Give the extent of all uninfected red blood cells.
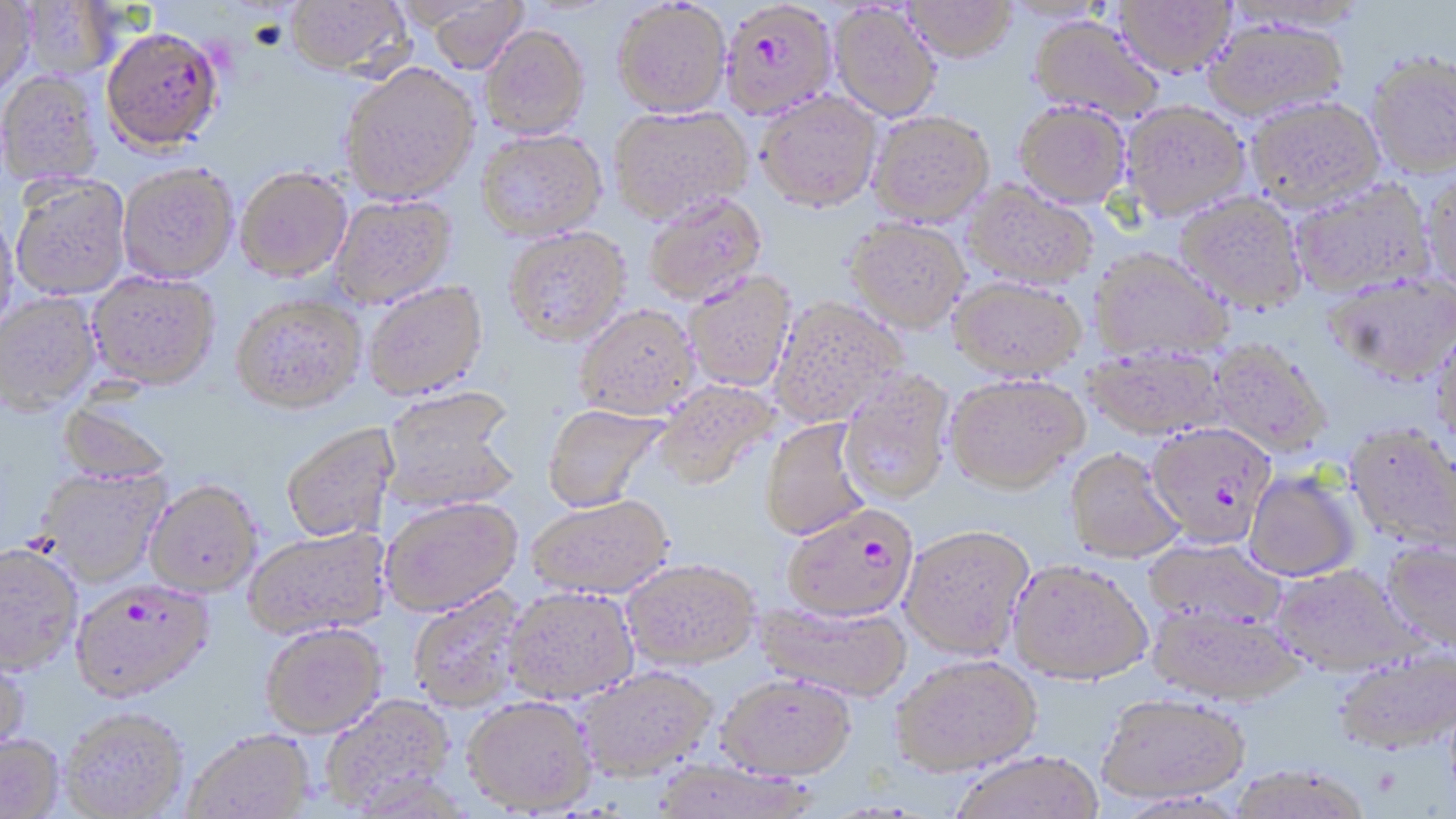

Approximate bounding boxes as [x1, y1, x2, y2] in pixels.
Uninfected red blood cells: [20, 0, 122, 80], [284, 0, 411, 78], [418, 0, 529, 74], [1114, 0, 1236, 77], [0, 1, 37, 98], [612, 1, 731, 117], [903, 1, 1017, 62], [1000, 1, 1118, 24], [1220, 1, 1371, 33], [829, 3, 941, 122], [1028, 16, 1163, 122], [1202, 18, 1349, 122], [479, 24, 590, 139], [1366, 51, 1456, 179], [339, 62, 479, 204], [0, 71, 104, 189], [756, 92, 882, 211], [1246, 95, 1384, 211], [1014, 101, 1131, 208], [1121, 102, 1251, 220], [608, 105, 753, 223], [868, 110, 994, 227], [476, 129, 606, 241], [117, 164, 239, 284], [235, 167, 352, 282], [1421, 173, 1456, 294], [10, 175, 131, 301], [1288, 179, 1435, 297], [962, 181, 1098, 291], [1177, 192, 1308, 312], [643, 193, 767, 305], [330, 195, 457, 308], [0, 209, 20, 338], [843, 217, 971, 332], [504, 227, 631, 346], [1089, 248, 1234, 363], [87, 271, 220, 390], [683, 271, 796, 392], [1324, 272, 1456, 385], [948, 276, 1087, 380], [363, 282, 488, 401], [0, 292, 101, 415], [230, 296, 367, 416], [770, 297, 909, 425], [575, 304, 699, 419], [1430, 325, 1456, 450], [1207, 337, 1333, 458], [1083, 346, 1227, 439], [838, 370, 956, 505], [945, 373, 1089, 493], [654, 379, 780, 489], [380, 390, 521, 512], [56, 394, 176, 487], [543, 404, 668, 511], [760, 418, 871, 540], [280, 421, 400, 543], [1345, 421, 1456, 552], [1065, 448, 1185, 563], [36, 468, 171, 588], [1243, 470, 1360, 581], [145, 480, 263, 598], [528, 494, 674, 598], [381, 497, 523, 616], [899, 524, 1034, 659], [243, 526, 392, 641], [1143, 538, 1287, 630], [1381, 541, 1456, 653], [0, 544, 83, 677], [623, 558, 759, 668], [1007, 559, 1152, 684], [1271, 563, 1420, 676], [409, 586, 529, 713], [503, 586, 639, 703], [754, 599, 912, 701], [1147, 603, 1305, 705], [260, 624, 387, 740], [1332, 649, 1456, 756], [0, 652, 30, 763], [891, 653, 1042, 775], [577, 666, 715, 780], [717, 673, 856, 779], [1096, 693, 1250, 803], [320, 694, 456, 812], [462, 696, 597, 815], [60, 709, 189, 818], [183, 729, 315, 818], [0, 735, 64, 819], [947, 750, 1105, 819], [649, 759, 819, 818], [1227, 764, 1374, 819].

Summary:
  - Plasmodium falciparum-infected red blood cell locations: [720, 1, 837, 119], [99, 27, 224, 152], [1146, 421, 1276, 546], [781, 505, 918, 621], [70, 580, 214, 704]
  - Slide-level diagnosis: Plasmodium falciparum
  - Stain: May-Grünwald-Giemsa
  - Field of view: single
  - Modality: light microscopy
  - Preparation: thin blood smear
  - Magnification: 1000x
  - Image size: 1456×819 pixels